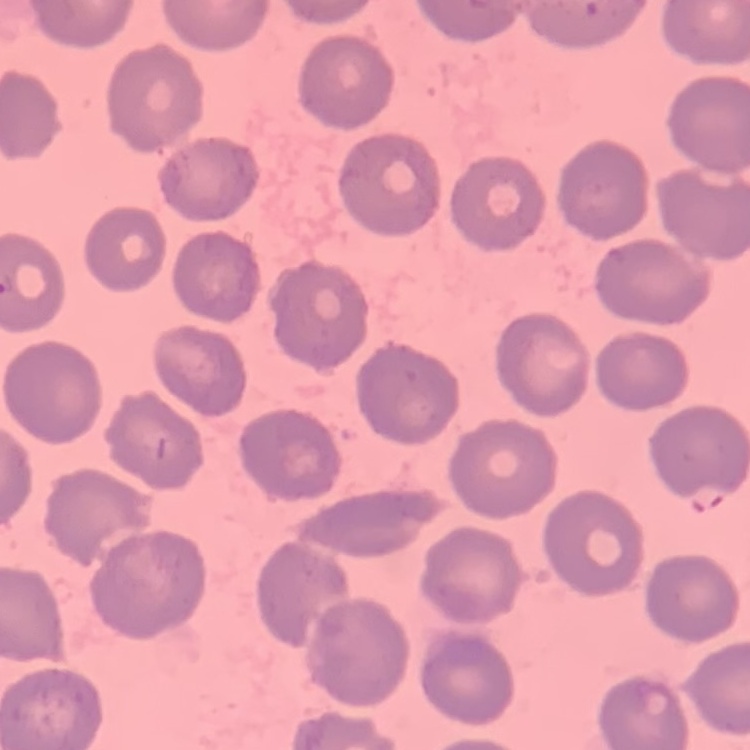
Summary:
  - Red blood cell morphology: no rouleaux formation
  - Stain: Field's or Giemsa
  - Preparation: thin blood smear
  - Image type: square crop of a larger photomicrograph